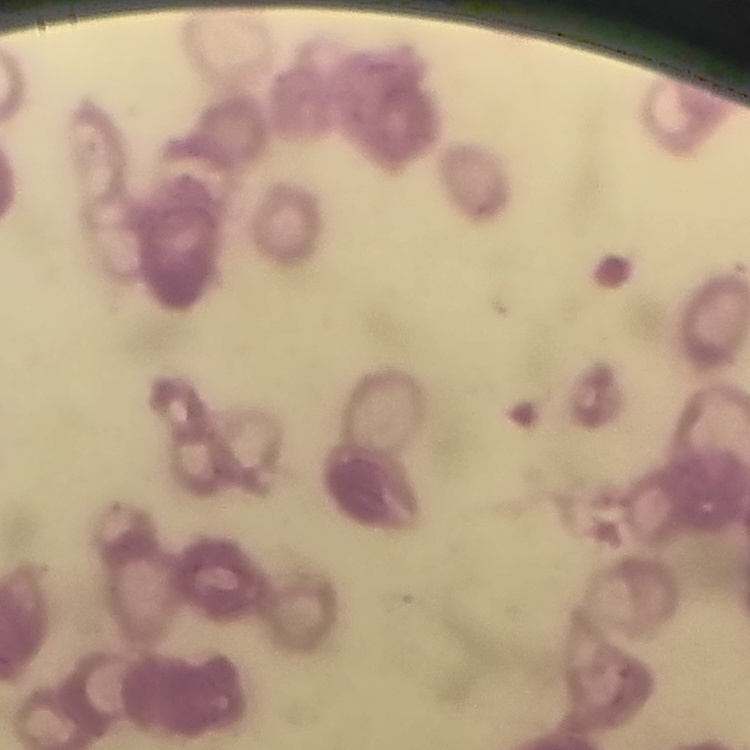 The erythrocytes exhibit rouleaux formation. Square crop of a larger photomicrograph. Field's or Giemsa stain. Thin peripheral smear.